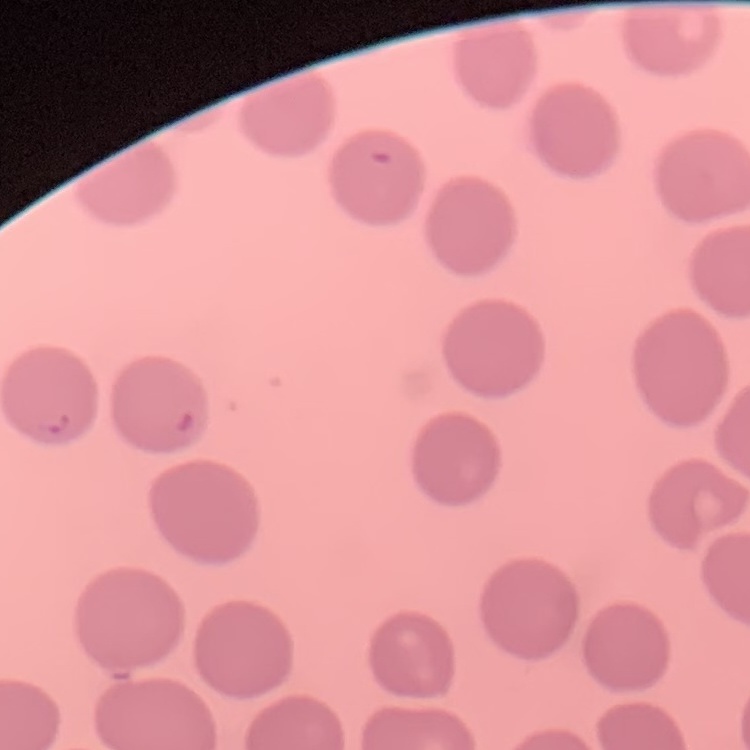 The erythrocytes exhibit no rouleaux formation. Thin blood film. Stained with either Field's or Giemsa. One tile cut from a larger photomicrograph.